Describe the morphology of the red blood cells.
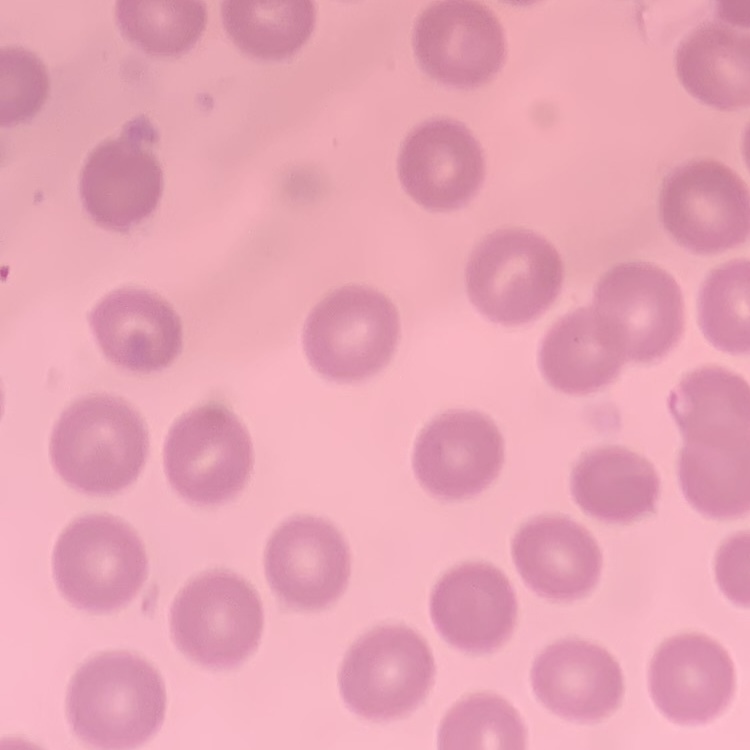
No rouleaux formation.

stain = Field's or Giemsa
preparation = thin blood smear
image type = one tile cut from a larger photomicrograph